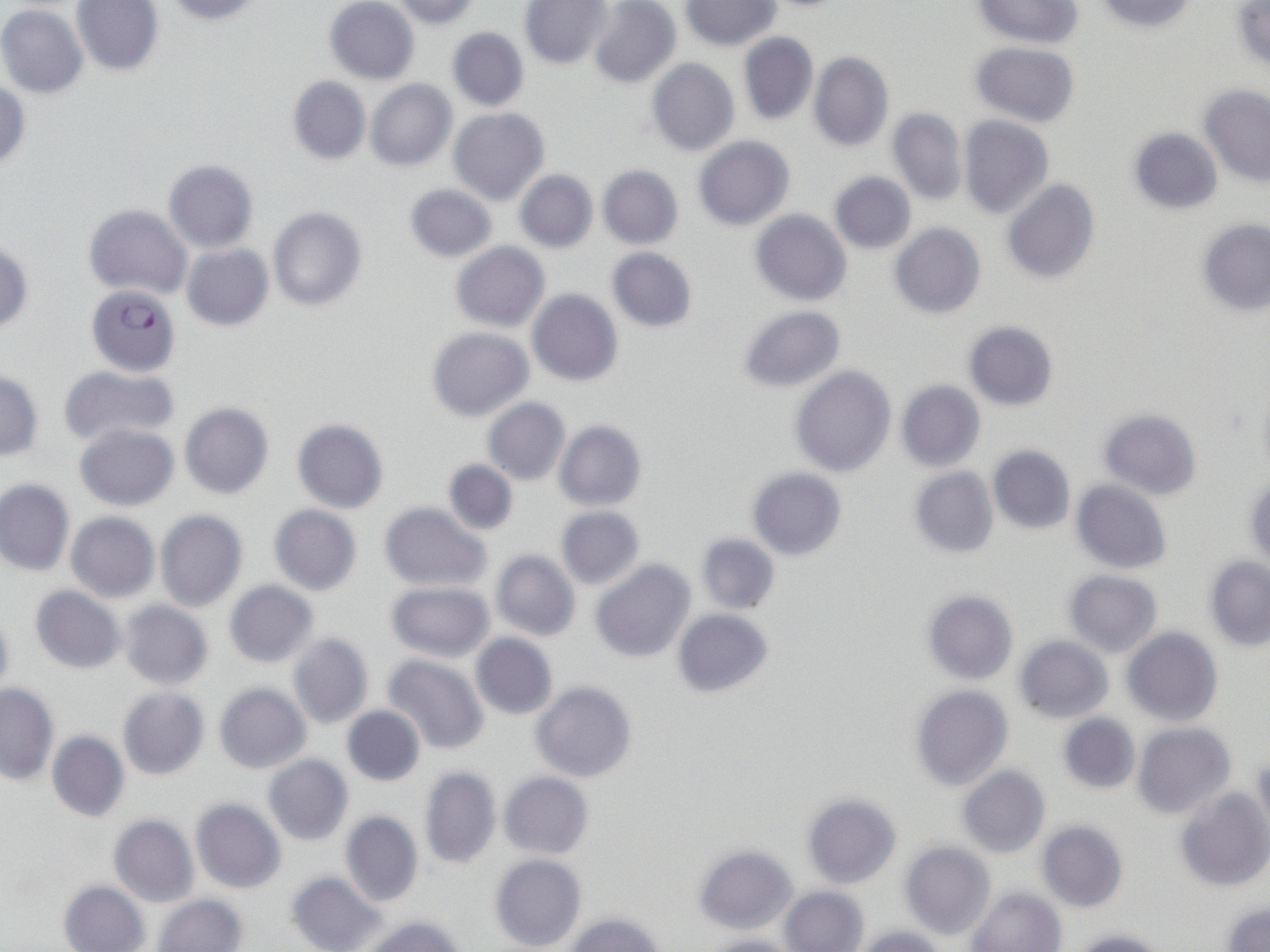

Summary:
  - Coordinate format: approximate bounding boxes as named x1/y1/x2/y2 corners in pixels
  - Plasmodium falciparum-infected red blood cell locations: (x1=86, y1=283, x2=181, y2=377)
  - Uninfected red blood cell locations: (x1=165, y1=0, x2=265, y2=25), (x1=586, y1=0, x2=681, y2=88), (x1=971, y1=0, x2=1081, y2=47), (x1=1092, y1=0, x2=1199, y2=33), (x1=71, y1=1, x2=165, y2=75), (x1=324, y1=1, x2=419, y2=84), (x1=388, y1=1, x2=481, y2=29), (x1=681, y1=1, x2=780, y2=50), (x1=520, y1=2, x2=614, y2=70), (x1=1230, y1=3, x2=1270, y2=71), (x1=0, y1=4, x2=88, y2=98), (x1=447, y1=27, x2=529, y2=111), (x1=737, y1=32, x2=819, y2=126), (x1=971, y1=41, x2=1080, y2=127), (x1=808, y1=51, x2=894, y2=150), (x1=646, y1=58, x2=740, y2=156), (x1=287, y1=75, x2=371, y2=164), (x1=1, y1=78, x2=30, y2=172), (x1=365, y1=79, x2=457, y2=170), (x1=1199, y1=84, x2=1270, y2=186), (x1=448, y1=107, x2=549, y2=205), (x1=887, y1=108, x2=967, y2=203), (x1=958, y1=115, x2=1054, y2=218), (x1=1126, y1=127, x2=1223, y2=215), (x1=692, y1=137, x2=795, y2=231), (x1=162, y1=159, x2=258, y2=253), (x1=597, y1=164, x2=683, y2=249), (x1=514, y1=170, x2=597, y2=252), (x1=828, y1=171, x2=916, y2=254), (x1=1000, y1=178, x2=1101, y2=284), (x1=403, y1=183, x2=497, y2=263), (x1=84, y1=204, x2=191, y2=298), (x1=268, y1=206, x2=368, y2=311), (x1=750, y1=209, x2=851, y2=306), (x1=1196, y1=218, x2=1270, y2=316), (x1=889, y1=223, x2=986, y2=319), (x1=452, y1=242, x2=550, y2=332), (x1=0, y1=243, x2=33, y2=336), (x1=182, y1=245, x2=273, y2=330), (x1=605, y1=248, x2=699, y2=331), (x1=527, y1=289, x2=623, y2=386), (x1=735, y1=305, x2=847, y2=392), (x1=962, y1=321, x2=1059, y2=411), (x1=427, y1=328, x2=532, y2=422), (x1=57, y1=364, x2=180, y2=447), (x1=790, y1=366, x2=897, y2=477), (x1=0, y1=371, x2=44, y2=462), (x1=895, y1=380, x2=985, y2=472), (x1=1255, y1=382, x2=1270, y2=479), (x1=483, y1=399, x2=570, y2=484), (x1=180, y1=402, x2=273, y2=499), (x1=1098, y1=407, x2=1203, y2=501), (x1=292, y1=418, x2=389, y2=513), (x1=554, y1=421, x2=646, y2=511), (x1=75, y1=423, x2=178, y2=510), (x1=987, y1=445, x2=1076, y2=534), (x1=443, y1=459, x2=518, y2=535), (x1=746, y1=467, x2=847, y2=560), (x1=908, y1=467, x2=999, y2=559), (x1=1244, y1=472, x2=1269, y2=569), (x1=0, y1=480, x2=75, y2=576), (x1=1072, y1=480, x2=1172, y2=575), (x1=379, y1=503, x2=490, y2=590), (x1=267, y1=505, x2=362, y2=596), (x1=554, y1=506, x2=644, y2=589), (x1=156, y1=509, x2=248, y2=612), (x1=66, y1=512, x2=159, y2=602), (x1=695, y1=533, x2=780, y2=615), (x1=490, y1=550, x2=581, y2=642), (x1=1204, y1=557, x2=1270, y2=651), (x1=589, y1=558, x2=695, y2=663), (x1=1062, y1=571, x2=1163, y2=657), (x1=223, y1=581, x2=320, y2=668), (x1=385, y1=582, x2=494, y2=662), (x1=30, y1=586, x2=125, y2=674), (x1=921, y1=588, x2=1018, y2=684), (x1=119, y1=601, x2=214, y2=689), (x1=0, y1=605, x2=15, y2=699), (x1=673, y1=609, x2=774, y2=698), (x1=1122, y1=628, x2=1222, y2=727), (x1=288, y1=633, x2=374, y2=728), (x1=470, y1=633, x2=558, y2=719), (x1=1013, y1=636, x2=1114, y2=722), (x1=382, y1=654, x2=490, y2=753), (x1=530, y1=680, x2=638, y2=781), (x1=214, y1=683, x2=311, y2=772), (x1=0, y1=685, x2=59, y2=784), (x1=909, y1=685, x2=1013, y2=790), (x1=118, y1=687, x2=208, y2=780), (x1=342, y1=705, x2=425, y2=786), (x1=1057, y1=713, x2=1140, y2=794), (x1=1133, y1=722, x2=1236, y2=819), (x1=47, y1=730, x2=129, y2=822), (x1=1144, y1=752, x2=1253, y2=878), (x1=262, y1=755, x2=354, y2=845), (x1=1253, y1=756, x2=1270, y2=837), (x1=958, y1=765, x2=1050, y2=859), (x1=419, y1=767, x2=501, y2=867), (x1=500, y1=772, x2=594, y2=858), (x1=1176, y1=788, x2=1270, y2=892), (x1=801, y1=792, x2=902, y2=888), (x1=190, y1=799, x2=286, y2=893), (x1=340, y1=812, x2=423, y2=906), (x1=109, y1=815, x2=198, y2=906), (x1=1037, y1=821, x2=1128, y2=913), (x1=900, y1=842, x2=996, y2=940), (x1=693, y1=844, x2=798, y2=933), (x1=489, y1=853, x2=586, y2=952), (x1=286, y1=871, x2=383, y2=952), (x1=59, y1=882, x2=149, y2=952), (x1=780, y1=885, x2=869, y2=952), (x1=967, y1=887, x2=1066, y2=952), (x1=154, y1=894, x2=247, y2=952), (x1=1220, y1=903, x2=1270, y2=952), (x1=564, y1=912, x2=664, y2=952), (x1=362, y1=916, x2=466, y2=952), (x1=851, y1=926, x2=951, y2=952), (x1=1071, y1=929, x2=1169, y2=952), (x1=703, y1=934, x2=804, y2=952)
  - Slide-level diagnosis: Plasmodium falciparum
  - Field of view: one of a larger specimen
  - Magnification: 1000x
  - Image size: 1270×952 pixels
  - Modality: optical microscopy
  - Stain: May-Grünwald-Giemsa
  - Preparation: thin blood film